Locate every uninfected red blood cell.
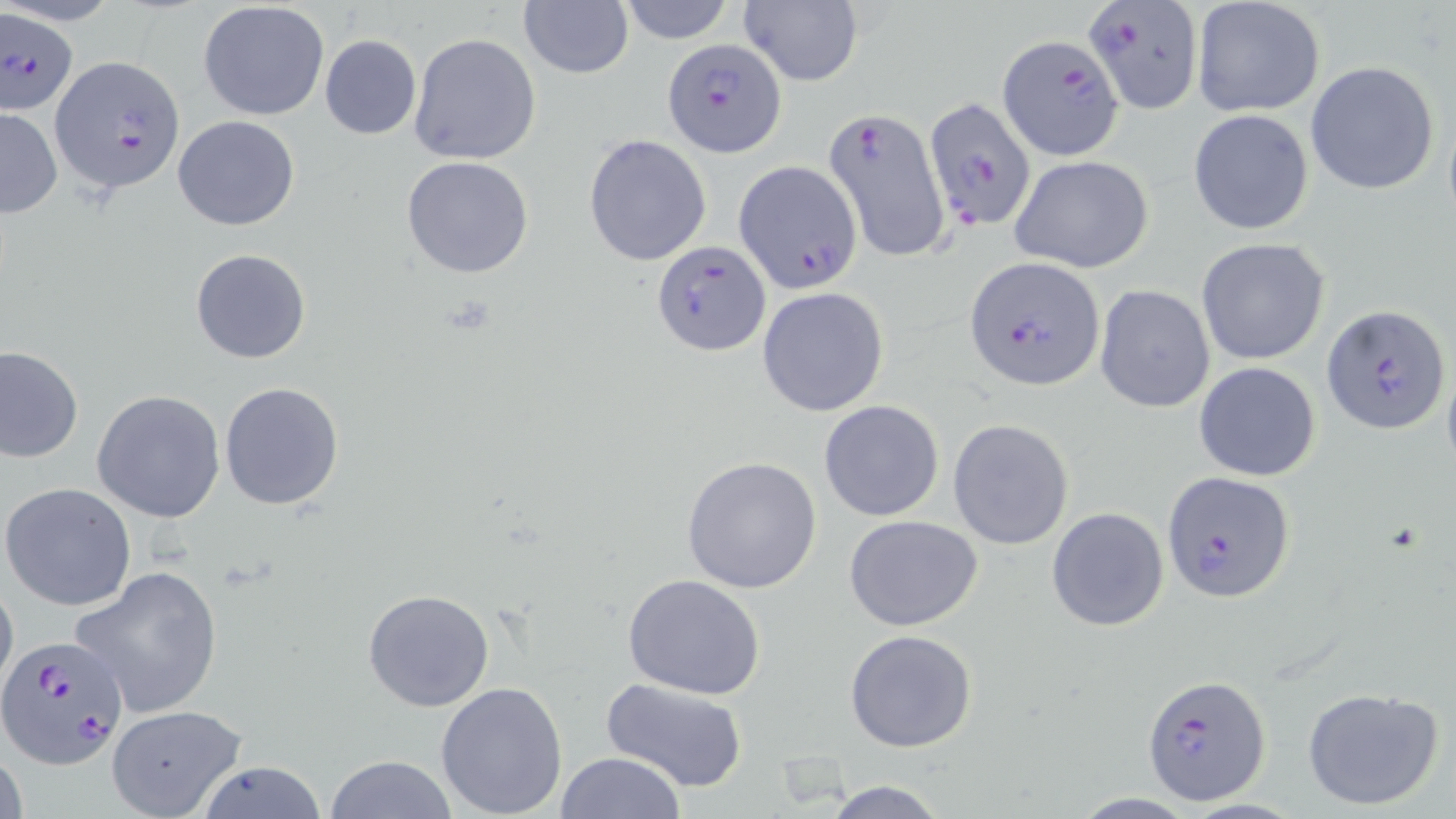
Approximate bounding boxes as (x1, y1, x2, y2) in pixels.
Uninfected red blood cells: (614, 0, 736, 44), (737, 0, 862, 88), (1191, 0, 1326, 119), (197, 1, 330, 121), (519, 2, 633, 79), (408, 33, 541, 165), (319, 34, 422, 140), (1306, 60, 1440, 195), (0, 107, 63, 218), (1187, 109, 1314, 236), (174, 115, 300, 232), (583, 134, 713, 267), (1010, 155, 1154, 273), (402, 156, 535, 279), (1197, 237, 1331, 365), (190, 248, 310, 363), (1095, 285, 1217, 414), (758, 287, 889, 416), (0, 345, 83, 463), (1194, 362, 1321, 482), (220, 381, 345, 511), (92, 388, 226, 523), (818, 401, 945, 520), (948, 417, 1075, 548), (680, 455, 824, 595), (1, 482, 137, 612), (1046, 505, 1169, 633), (842, 513, 985, 632), (68, 563, 226, 719), (0, 570, 18, 707), (622, 574, 768, 699), (362, 589, 496, 712), (845, 629, 978, 753), (600, 679, 751, 793), (434, 680, 569, 817), (1300, 686, 1444, 811), (105, 704, 248, 819), (2, 737, 27, 819), (554, 752, 687, 819), (321, 755, 462, 818), (193, 759, 329, 817), (817, 778, 955, 819).

{
  "slide_level_diagnosis": "Plasmodium falciparum",
  "image_size": "1456×819 pixels",
  "field_of_view": "one of a larger specimen",
  "modality": "optical microscopy",
  "stain": "May-Grünwald-Giemsa",
  "plasmodium_falciparum_infected_red_blood_cell_locations": "approximate bounding boxes as (x1, y1, x2, y2) in pixels: (1084, 0, 1203, 113), (0, 7, 81, 118), (999, 34, 1125, 160), (662, 37, 786, 155), (46, 55, 182, 197), (923, 97, 1038, 232), (824, 107, 953, 263), (734, 161, 862, 293), (652, 239, 772, 355), (963, 255, 1104, 393), (1322, 304, 1449, 434), (1162, 472, 1295, 601), (0, 635, 131, 770), (1143, 675, 1270, 804)",
  "magnification": "1000x",
  "preparation": "thin blood film"
}